Assess this cell for malaria.
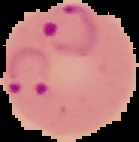
It is parasitized.

{
  "image_type": "cell region segmented out of the field of view; surrounding area masked to black",
  "image_size": "139×142 pixels",
  "preparation": "thin blood film"
}